Assess this cell for malaria.
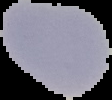
It is uninfected.

Summary:
  - Image size: 112×100 pixels
  - Image type: segmented cell region with the area outside set to black
  - Preparation: thin blood smear